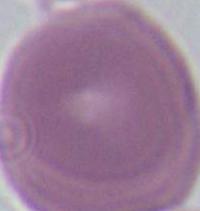

Summary:
  - Magnification: 1000x
  - Modality: photomicrograph
  - Identification: red blood cell